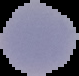
The area outside the segmented cell region is set to black. Image is 79×76 pixels. From a thin blood film. Malaria status: parasitized.